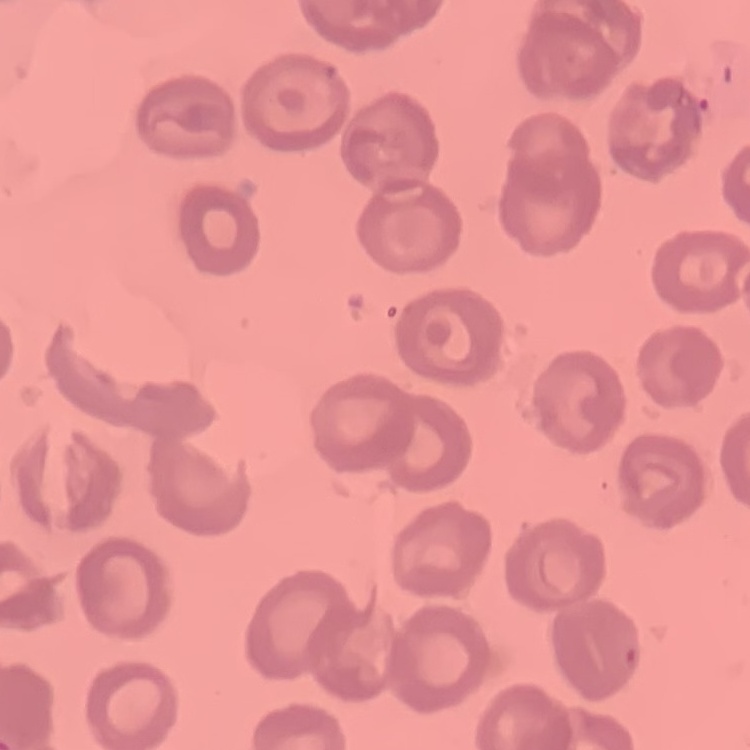
Summary:
  - Erythrocyte morphology: no rouleaux formation
  - Stain: Field's or Giemsa
  - Preparation: thin peripheral smear
  - Image type: square crop of a larger photomicrograph